Assess for Plasmodium parasites.
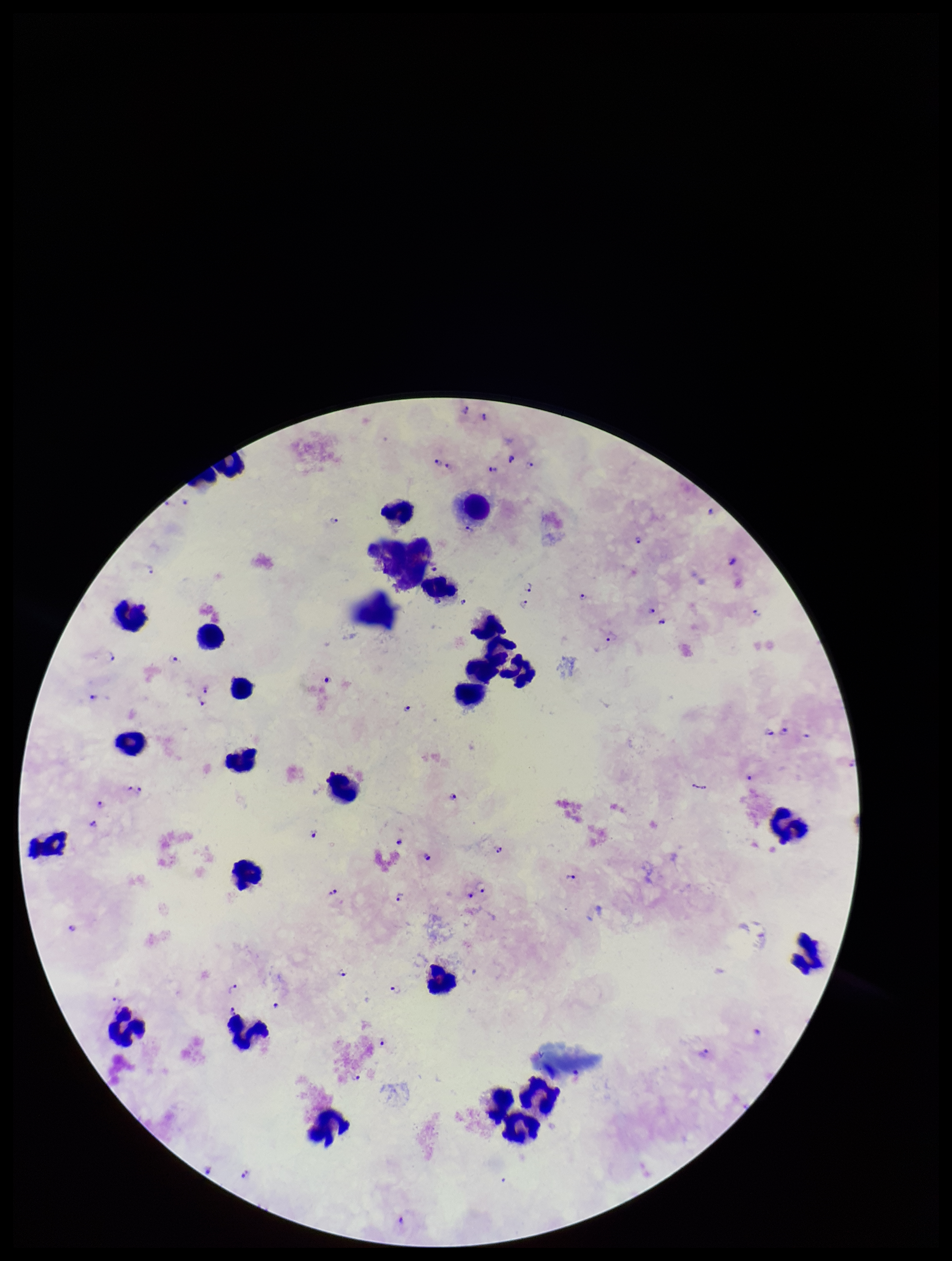

Detected.

Summary:
  - Image size: 952×1261 pixels
  - Patient malaria status: infected
  - Species reported for this patient: Plasmodium falciparum
  - Leukocyte count: 27
  - Stain: Giemsa
  - Preparation: thick blood smear
  - Parasite count: 66
  - Capture: smartphone photograph through the microscope eyepiece
  - Field of view: one from this slide